Report the malaria status of this cell.
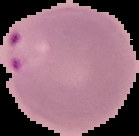
Parasitized.

Segmented cell region on a black background. Image is 139×136 pixels. From a thin blood film.